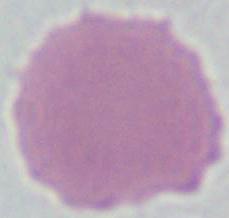
Summary:
  - Magnification: 1000x
  - Identification: erythrocyte
  - Modality: micrograph